Locate every Plasmodium parasite.
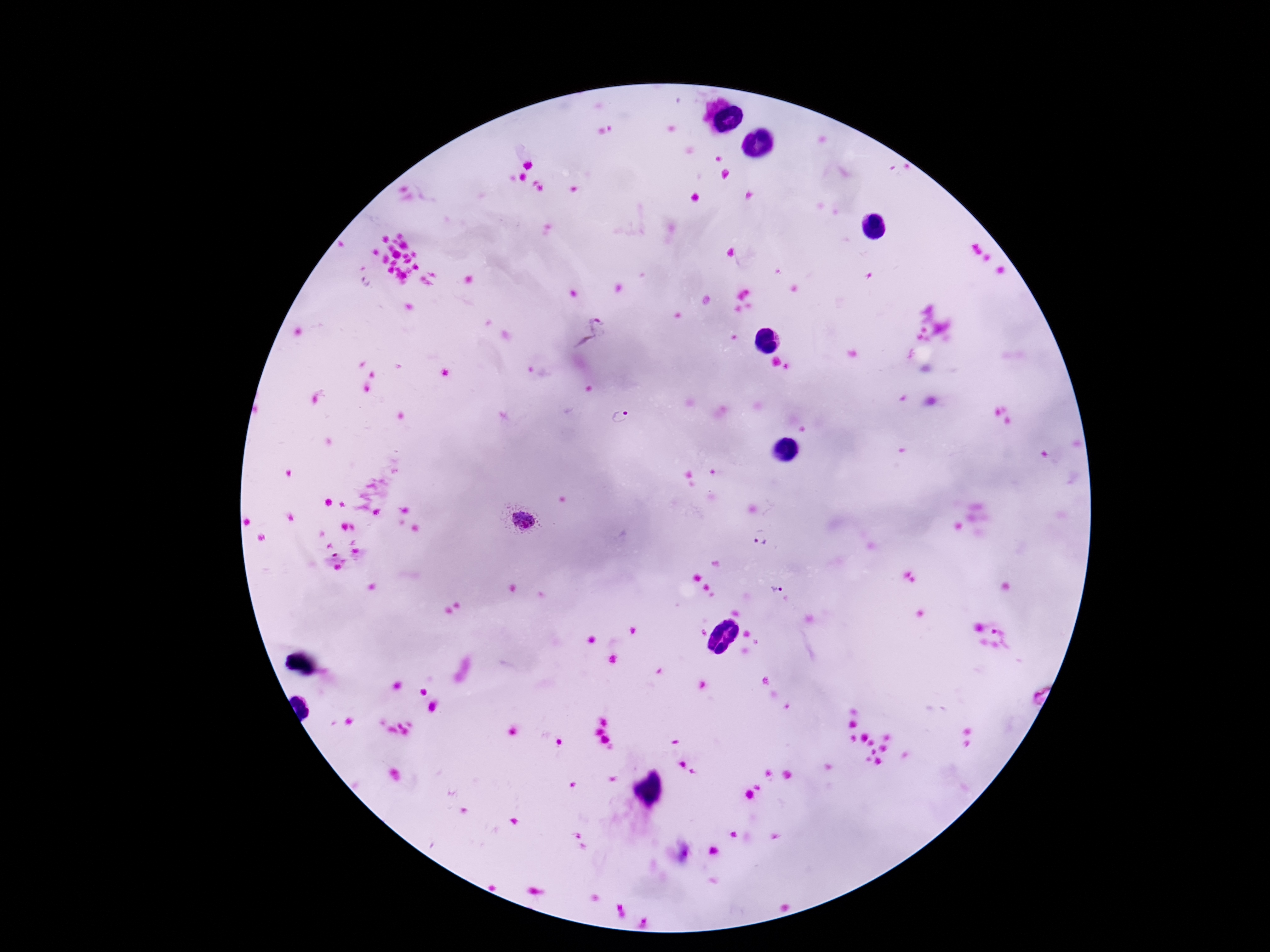

Approximate centers as {x, y} in pixels.
Plasmodium parasites: {589, 333}, {619, 418}, {524, 520}, {762, 536}, {776, 587}.

Summary:
  - Capture: smartphone camera through the microscope eyepiece
  - Image size: 1270×952 pixels
  - Field of view: one from this slide
  - Stain: Giemsa
  - Magnification: 100x
  - Preparation: thick blood smear
  - Patient malaria status: positive